Describe the morphology of the erythrocytes.
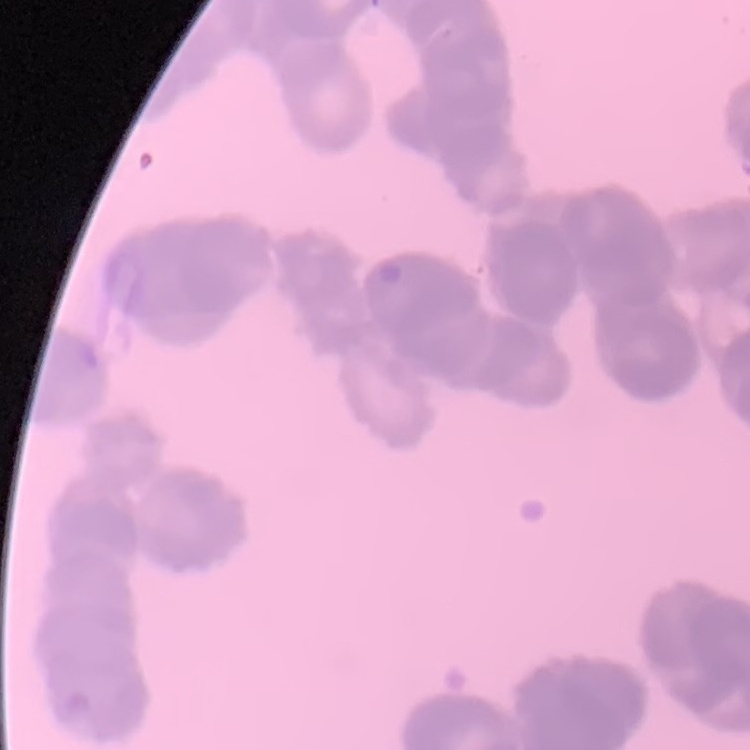

They show rouleaux formation.

Thin blood film. Stained with either Field's or Giemsa. One tile cut from a larger photomicrograph.